Report the malaria status of this cell.
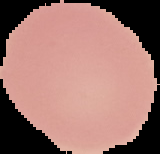
It is uninfected.

image_type: segmented cell region with the area outside set to black
preparation: thin blood film
image_size: 160×154 pixels